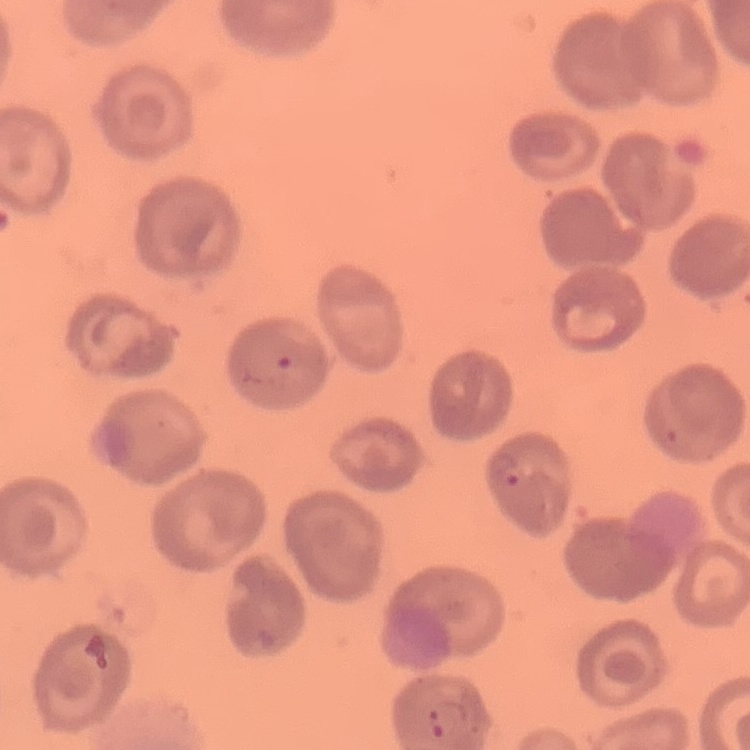
Summary:
  - Red blood cell morphology: no rouleaux formation
  - Preparation: thin blood smear
  - Image type: one tile cut from a larger photomicrograph
  - Stain: Field's or Giemsa